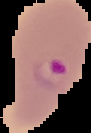
From a thin blood smear. The area outside the segmented cell region is set to black. Malaria status: parasitized. Image is 91×133 pixels.